Identify the parasite.
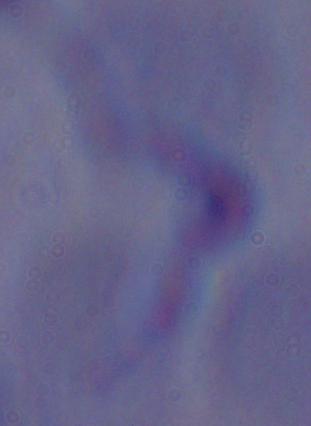

A trypanosome.

modality = photomicrograph
magnification = 1000x